Name the parasite shown.
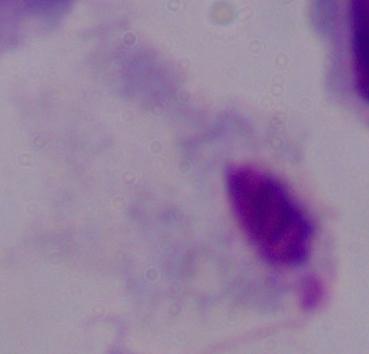

This is a trichomonad.

magnification = 1000x
modality = micrograph